Name the parasite shown.
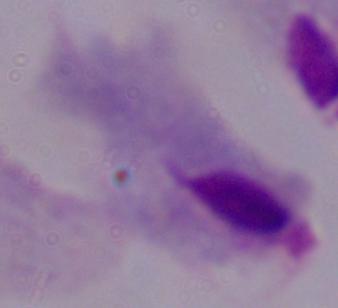

This is a trichomonad.

Summary:
  - Modality: micrograph
  - Magnification: 1000x